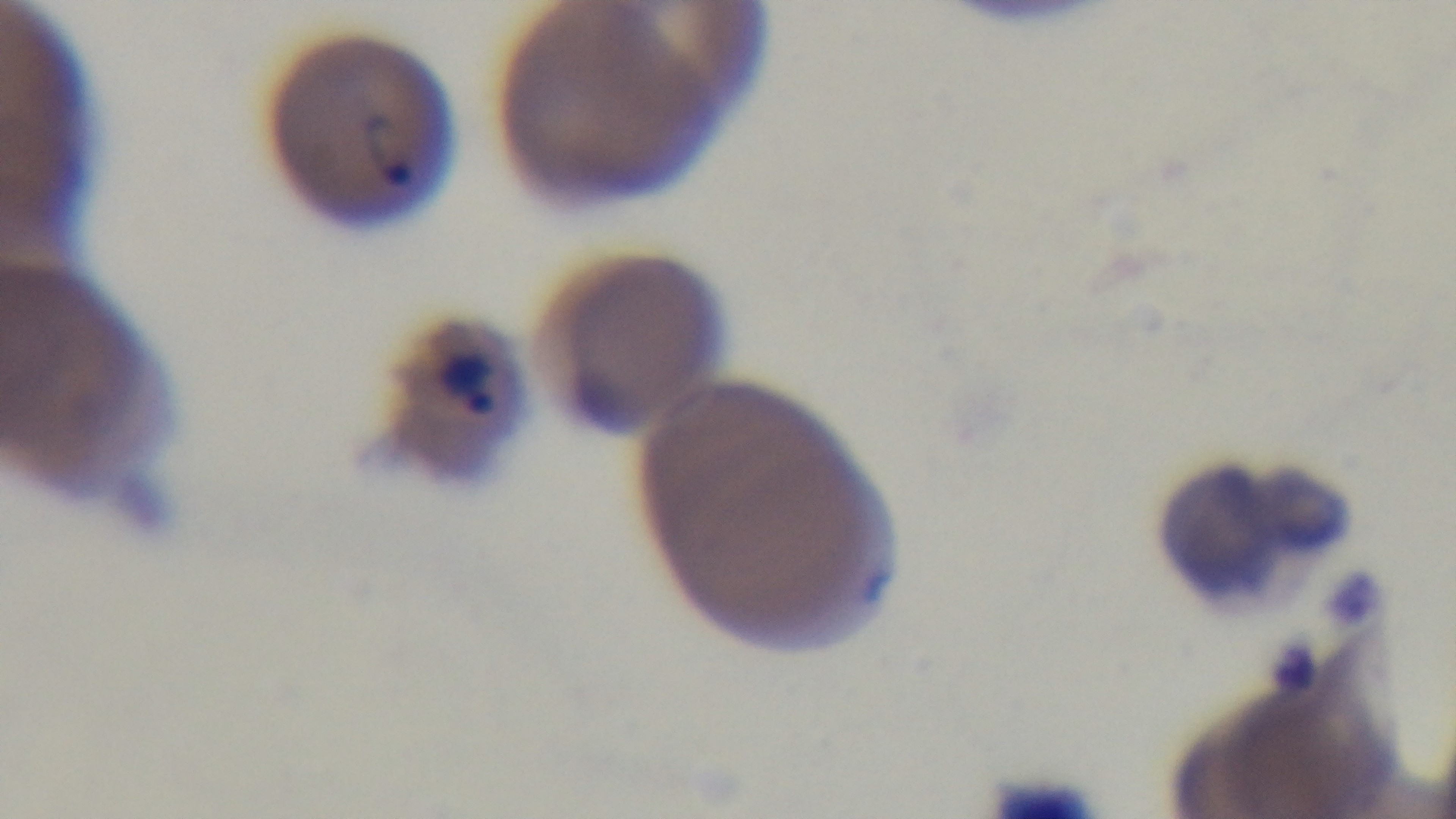

Giemsa-stained. Captured with a mounted 4K digital camera. 100x oil-immersion objective. Photomicrograph. Preparation: thin smear. Malaria status: infected. Single field of view.